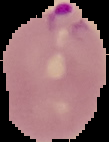

Summary:
  - Image size: 109×142 pixels
  - Preparation: thin blood film
  - Result: Plasmodium parasites detected
  - Image type: cell region segmented out of the field of view; surrounding area masked to black